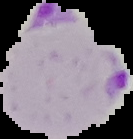
{
  "preparation": "thin blood film",
  "image_type": "cell region segmented out of the field of view; surrounding area masked to black",
  "image_size": "133×139 pixels",
  "malaria_status": "parasitized"
}